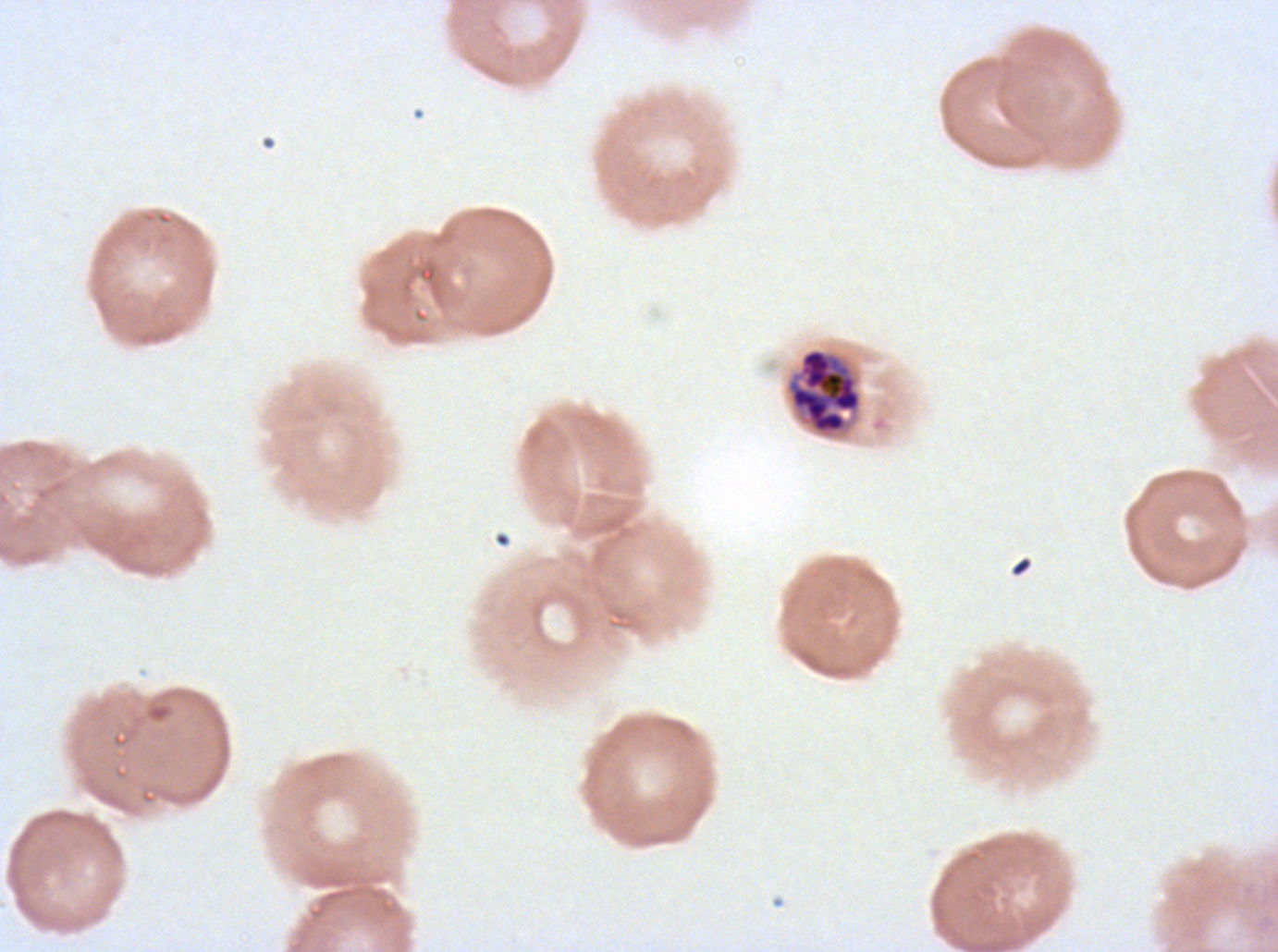

notation = approximate bounding boxes as {x1, y1, x2, y2} in pixels
segmenter locations = {786, 348, 862, 435}
field of view = sub-image separated from a larger composite
preparation = thin blood film
image size = 1278×952 pixels
specimen = Plasmodium falciparum from a patient in The Gambia, cultured ex vivo for 24 to 48 hours
stain = Giemsa